Assess the morphology of the erythrocytes.
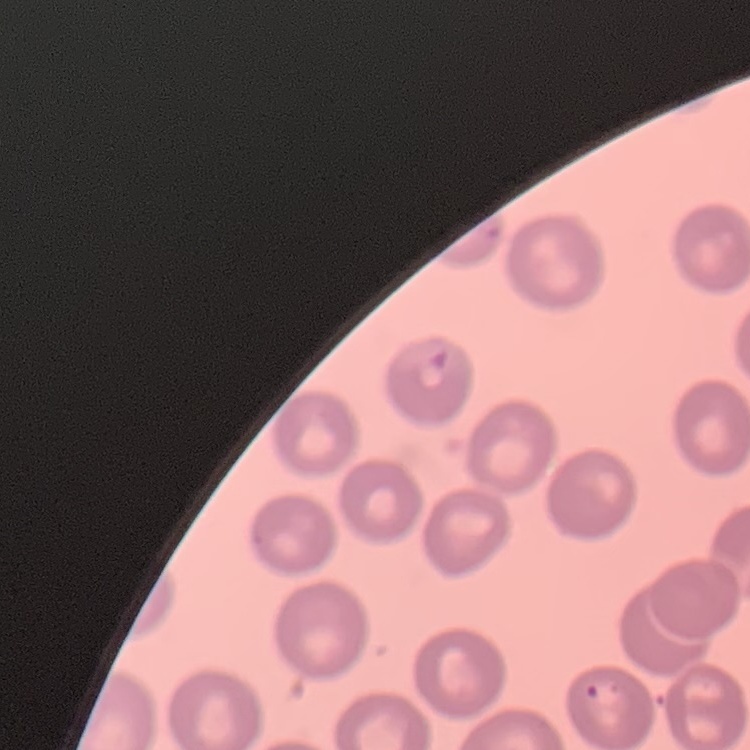
They show no rouleaux formation.

stain = Field's or Giemsa
preparation = thin peripheral smear
image type = one tile cut from a larger photomicrograph